Assess this cell for malaria.
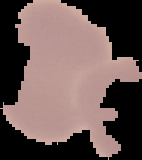
Uninfected.

{
  "preparation": "thin blood film",
  "image_size": "142×160 pixels",
  "image_type": "cell region segmented out of the field of view; surrounding area masked to black"
}